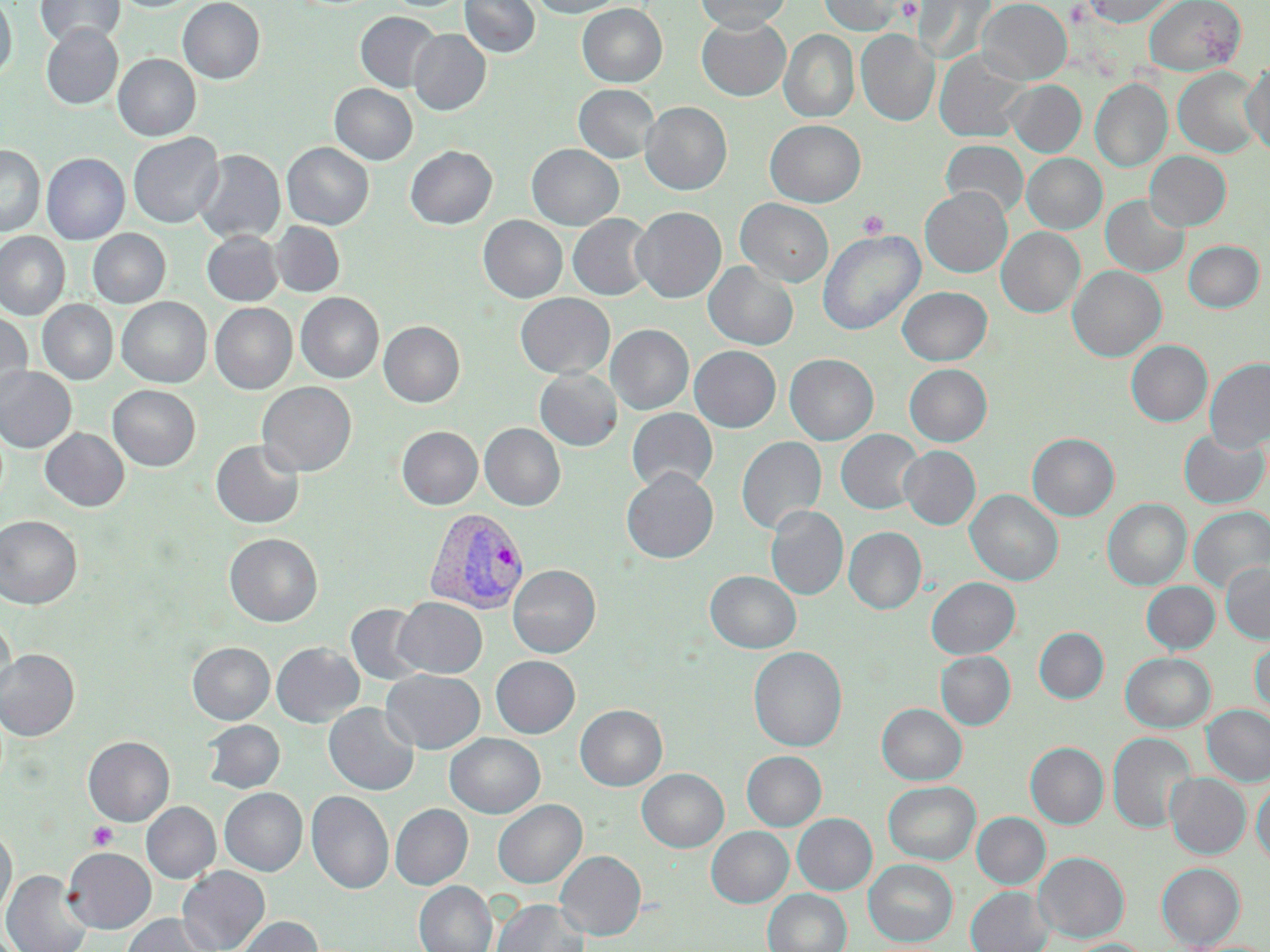

slide_level_diagnosis: Plasmodium vivax
field_of_view: single
magnification: 1000x
uninfected_red_blood_cell_locations: 'approximate bounding boxes as (x1,y1)-(x2,y2) corner pairs in pixels: (0,0)-(16,81), (34,0)-(125,49), (178,0)-(265,84), (383,0)-(470,12), (460,0)-(539,58), (532,0)-(624,18), (695,0)-(791,33), (817,0)-(916,36), (914,0)-(996,66), (977,0)-(1071,84), (1081,0)-(1179,27), (1144,0)-(1245,74), (577,4)-(667,87), (355,12)-(442,93), (696,16)-(791,101), (41,25)-(123,109), (408,29)-(491,116), (779,29)-(859,123), (856,30)-(939,126), (934,51)-(1029,143), (113,54)-(200,141), (1241,61)-(1270,157), (1173,67)-(1264,158), (1090,78)-(1172,172), (1006,80)-(1086,157), (330,84)-(417,165), (574,84)-(660,163), (640,102)-(732,195), (765,120)-(865,207), (128,133)-(224,228), (940,140)-(1028,219), (282,142)-(374,230), (527,144)-(623,230), (0,145)-(45,237), (406,146)-(497,229), (193,149)-(285,244), (1145,151)-(1231,231), (41,153)-(129,244), (1022,153)-(1107,233), (920,187)-(1012,277), (1101,194)-(1189,278), (736,199)-(833,286), (631,207)-(726,303), (567,214)-(655,301), (478,215)-(567,303), (270,221)-(345,297), (997,227)-(1085,319), (88,229)-(170,308), (817,230)-(925,336), (202,231)-(283,306), (0,232)-(70,320), (1184,240)-(1264,312), (703,262)-(798,350), (1067,265)-(1166,362), (897,286)-(993,366), (296,293)-(383,383), (515,293)-(615,379), (117,297)-(212,387), (37,300)-(117,384), (210,303)-(297,393), (0,312)-(32,403), (379,321)-(465,407), (606,324)-(693,415), (1126,340)-(1212,427), (689,346)-(781,432), (784,353)-(879,445), (1205,358)-(1270,451), (904,364)-(992,446), (0,366)-(76,452), (535,368)-(622,451), (258,382)-(356,476), (108,385)-(200,471), (627,408)-(718,492), (480,423)-(565,511), (397,426)-(482,509), (40,428)-(129,511), (1178,428)-(1269,509), (836,429)-(923,514), (1028,432)-(1119,521), (736,436)-(826,534), (211,439)-(305,529), (899,446)-(981,529), (621,468)-(719,563), (966,489)-(1063,586), (1103,498)-(1191,591), (766,505)-(848,600), (1188,506)-(1270,593), (0,516)-(82,608), (844,527)-(926,614), (225,533)-(323,627), (1221,562)-(1270,643), (507,565)-(601,658), (705,571)-(801,653), (927,577)-(1020,659), (1141,581)-(1220,654), (394,598)-(486,678), (346,604)-(429,685), (0,618)-(15,704), (1035,627)-(1109,704), (1250,634)-(1270,715), (187,642)-(275,724), (271,642)-(364,727), (748,646)-(847,752), (0,649)-(79,740), (936,651)-(1015,730), (1121,652)-(1216,733), (491,655)-(580,738), (381,669)-(485,754), (324,703)-(419,796), (877,703)-(966,785), (575,704)-(667,791), (1201,705)-(1270,786), (202,720)-(285,793), (1108,732)-(1195,834), (445,733)-(545,818), (83,736)-(174,826), (1026,742)-(1108,829), (742,751)-(826,830), (637,768)-(728,853), (1165,772)-(1251,859), (1252,779)-(1270,866), (883,781)-(981,865), (219,788)-(307,876), (306,790)-(394,894), (492,800)-(587,888), (141,802)-(220,883), (390,804)-(473,889), (972,812)-(1050,889), (792,813)-(877,895), (0,826)-(16,923), (706,826)-(794,908), (63,847)-(156,933), (555,851)-(646,940), (1034,851)-(1129,942), (863,859)-(958,946), (1156,862)-(1245,949), (177,866)-(270,952), (2,869)-(92,952), (414,881)-(497,952), (965,886)-(1054,952), (762,888)-(851,952), (492,898)-(589,952), (119,913)-(223,952), (235,915)-(322,952), (1066,938)-(1150,952)'
stain: May-Grünwald-Giemsa
preparation: thin blood smear
modality: optical microscopy
plasmodium_vivax_infected_red_blood_cell_locations: 'approximate bounding boxes as (x1,y1)-(x2,y2) corner pairs in pixels: (424,507)-(530,614)'
platelet_locations: 'approximate bounding boxes as (x1,y1)-(x2,y2) corner pairs in pixels: (858,210)-(889,239), (86,822)-(118,850)'
image_size: 1270×952 pixels